Classify this cell by malaria status.
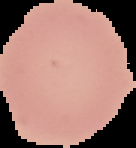

It is uninfected.

Summary:
  - Image type: segmented cell region on a black background
  - Image size: 136×148 pixels
  - Preparation: thin blood smear